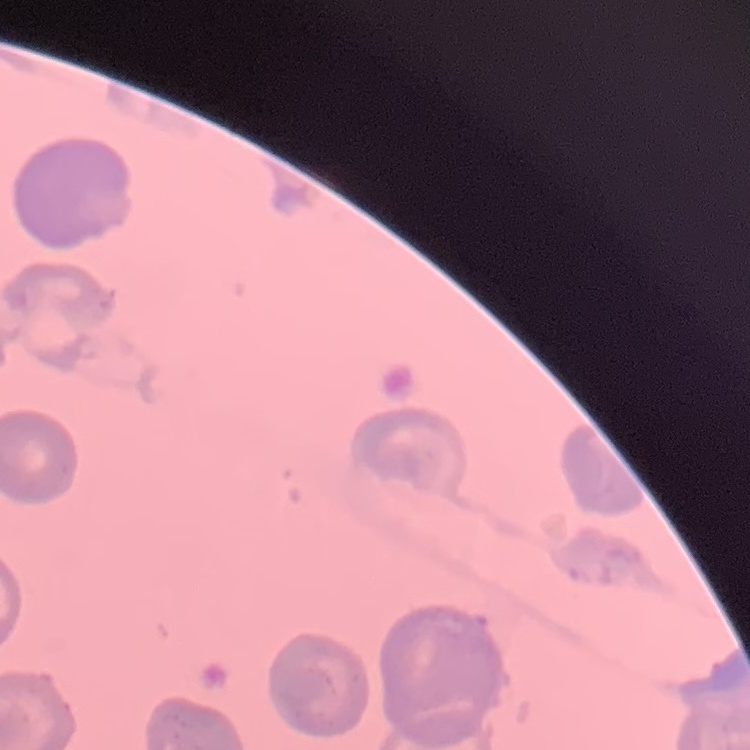

red blood cell morphology = no rouleaux formation
stain = Field's or Giemsa
image type = one tile cut from a larger photomicrograph
preparation = thin peripheral smear